Locate every blood parasite and identify its species.
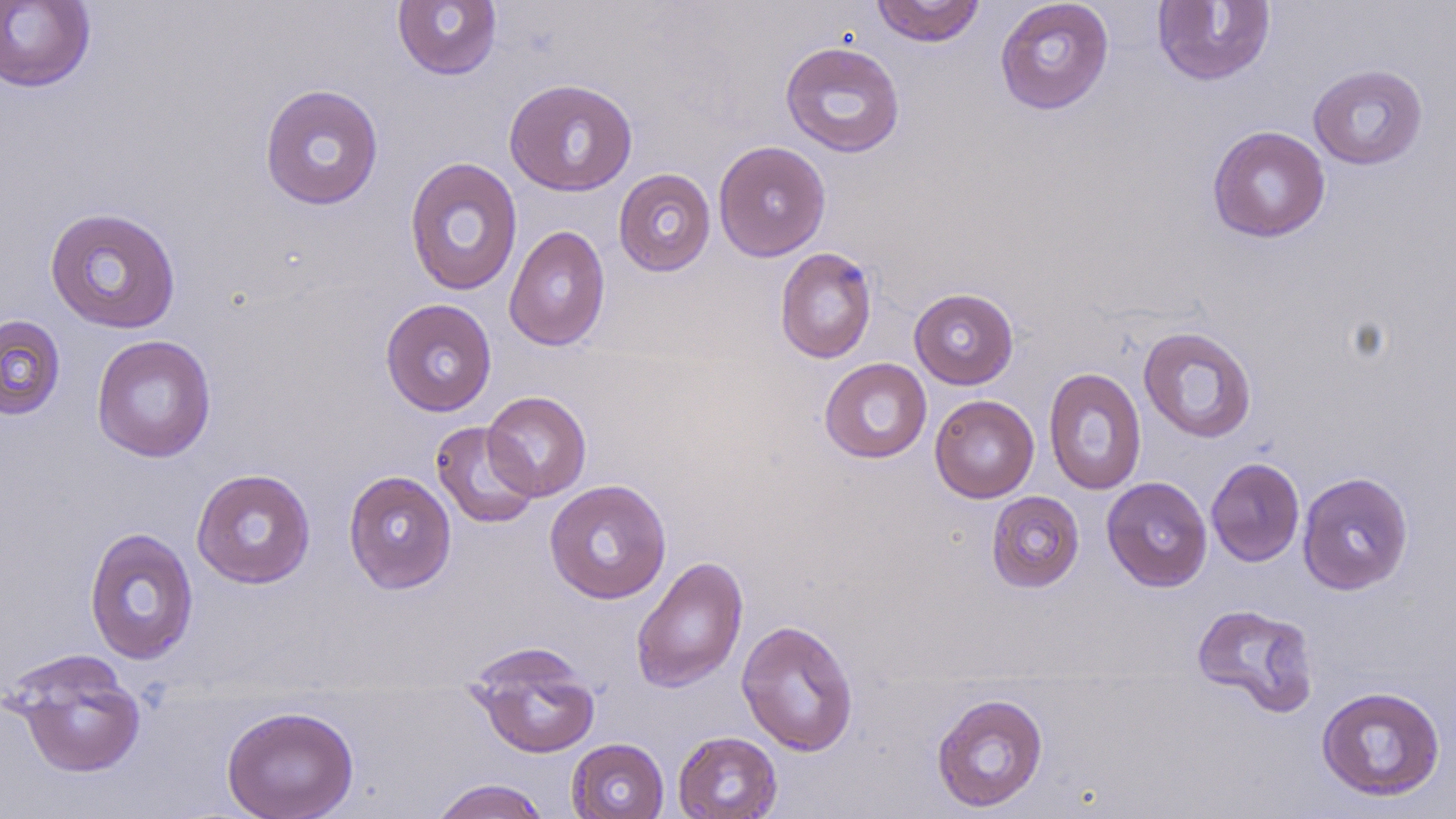

No blood parasites seen.

Summary:
  - Coordinate format: approximate bounding boxes as [x1, y1, x2, y2] in pixels
  - Uninfected red blood cell locations: [871, 0, 985, 47], [994, 0, 1114, 115], [0, 1, 95, 93], [392, 1, 502, 80], [1151, 1, 1276, 87], [779, 41, 906, 157], [1308, 64, 1428, 170], [504, 78, 638, 196], [259, 83, 384, 210], [1207, 125, 1331, 242], [713, 140, 831, 262], [404, 156, 523, 296], [613, 169, 716, 277], [44, 205, 182, 334], [504, 225, 611, 352], [774, 247, 878, 364], [908, 287, 1019, 389], [380, 298, 497, 417], [0, 314, 66, 420], [1138, 326, 1257, 443], [91, 334, 216, 463], [819, 358, 932, 464], [1043, 367, 1147, 495], [482, 391, 591, 501], [929, 395, 1039, 503], [431, 421, 541, 528], [1206, 457, 1305, 567], [191, 468, 316, 589], [343, 470, 457, 593], [1297, 471, 1414, 595], [1102, 476, 1213, 592], [544, 479, 672, 604], [986, 490, 1084, 593], [84, 527, 199, 665], [630, 555, 749, 693], [1191, 602, 1319, 718], [736, 619, 859, 756], [466, 643, 600, 759], [4, 649, 147, 778], [1316, 685, 1446, 802], [932, 692, 1049, 812], [221, 705, 359, 819], [673, 730, 782, 818], [567, 738, 669, 818], [431, 778, 551, 819]
  - Slide-level diagnosis: negative for blood parasites
  - Field of view: one of a larger specimen
  - Preparation: thin blood film
  - Stain: May-Grünwald-Giemsa
  - Modality: light microscopy
  - Magnification: 1000x
  - Image size: 1456×819 pixels